Assess the morphology of the red blood cells.
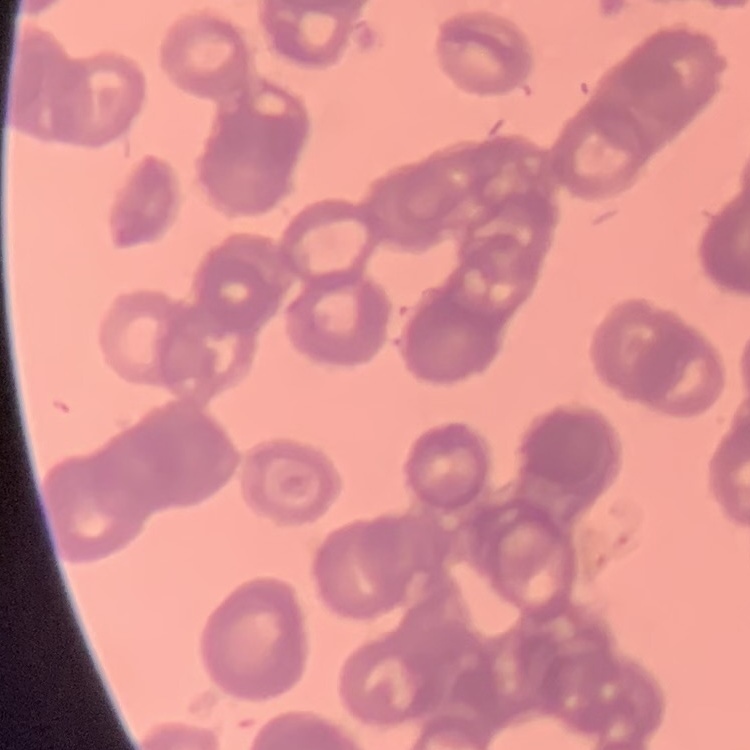
Rouleaux formation.

stain = Field's or Giemsa
image type = one tile cut from a larger photomicrograph
preparation = thin peripheral smear